State which cell type is depicted.
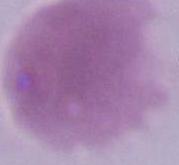

An erythrocyte.

modality: photomicrograph
magnification: 1000x